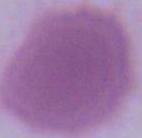

identification: red blood cell
magnification: 1000x
modality: micrograph